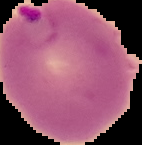

{
  "image_type": "segmented cell region on a black background",
  "image_size": "142×145 pixels",
  "preparation": "thin blood smear",
  "result": "Plasmodium parasites identified"
}